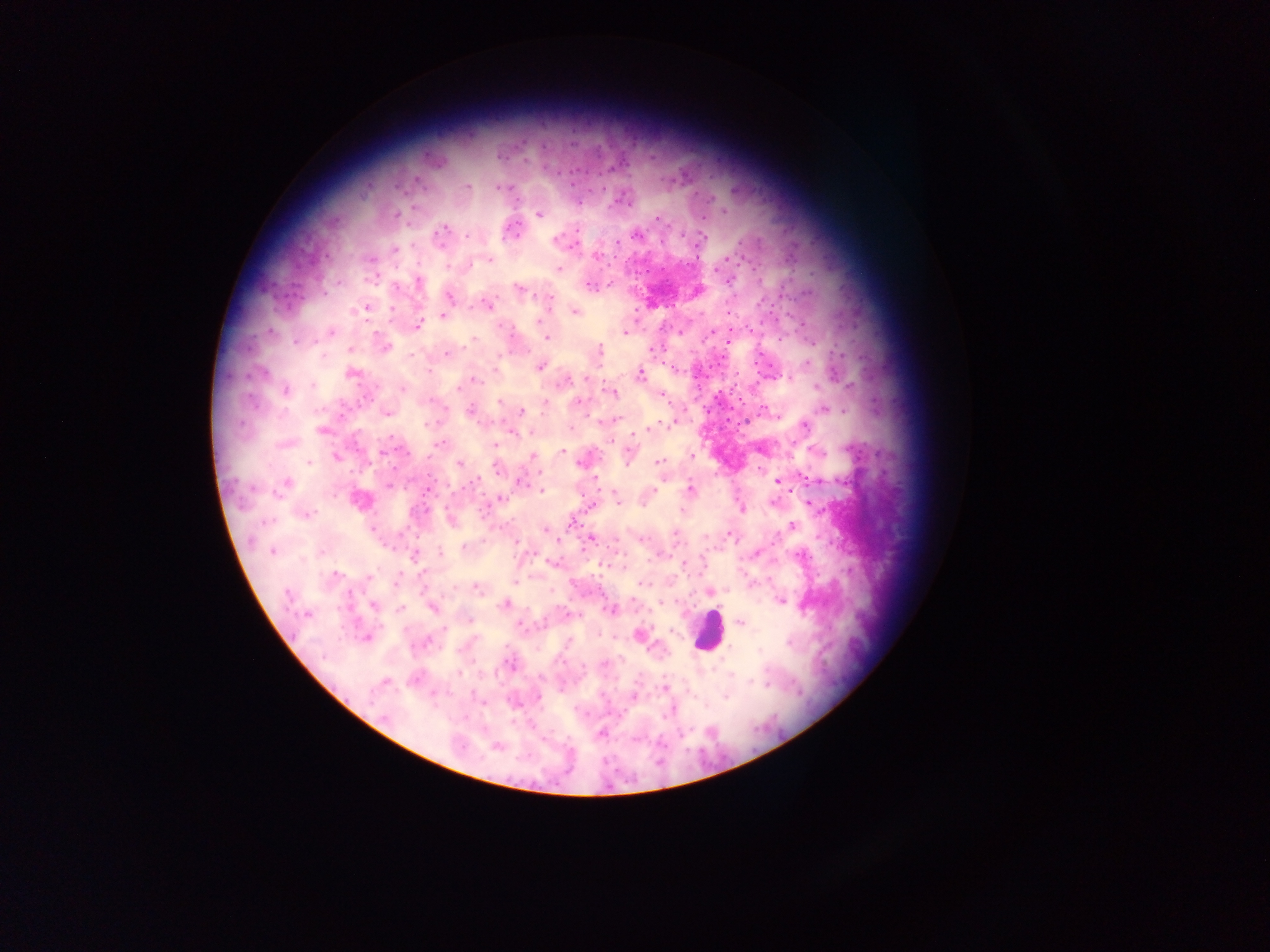 Approximate centers as (x, y) in pixels. Plasmodium parasite locations: (498, 156), (415, 179), (467, 187), (497, 187), (414, 208), (539, 214), (396, 216), (657, 218), (446, 228), (578, 230), (635, 234), (438, 237), (467, 237), (701, 238), (556, 240), (617, 243), (411, 245), (395, 248), (597, 256), (370, 259), (725, 259), (489, 260), (471, 264), (447, 266), (559, 269), (728, 281), (418, 282), (589, 286), (518, 288), (449, 296), (549, 298), (487, 305), (365, 309), (392, 309), (575, 312), (442, 316), (539, 321), (417, 326), (503, 327), (625, 332), (331, 333), (710, 333), (546, 338), (472, 340), (295, 342), (384, 348), (350, 349), (599, 352), (447, 354), (322, 356), (410, 356), (499, 357), (807, 364), (541, 366), (352, 374), (640, 374), (585, 378), (787, 378), (474, 380), (566, 381), (313, 384), (815, 386), (849, 386), (459, 388), (403, 389), (286, 391), (611, 392), (661, 395), (432, 399), (499, 402), (577, 402), (545, 404), (823, 409), (470, 411), (521, 411), (387, 414), (615, 420), (430, 423), (667, 423), (805, 426), (647, 428), (321, 430), (284, 444), (439, 444), (495, 445), (563, 451), (815, 452), (383, 453), (692, 455), (532, 456), (628, 456), (337, 458), (658, 461), (309, 462), (579, 462), (460, 464), (497, 469), (595, 478), (803, 478), (808, 480), (522, 481), (777, 481), (475, 482), (285, 483), (388, 484), (428, 488), (690, 489), (278, 490), (542, 491), (654, 491), (501, 499), (618, 500), (772, 502), (808, 504), (742, 508), (681, 510), (306, 514), (451, 521), (793, 526), (545, 530), (675, 534), (729, 534), (643, 538), (591, 539), (516, 543), (464, 547), (272, 551), (441, 552), (756, 553), (799, 555), (413, 556), (683, 564), (336, 574), (369, 576), (395, 583), (643, 584), (477, 589), (710, 592), (287, 595), (781, 600), (506, 604), (661, 604), (373, 605), (432, 608), (400, 609), (610, 610), (307, 615), (470, 620), (740, 623), (520, 625), (445, 628), (640, 634), (366, 637), (568, 642), (788, 643), (759, 651), (512, 663), (604, 663), (459, 673), (385, 681), (752, 681), (765, 685), (664, 688), (633, 696), (538, 697), (726, 697), (384, 717), (601, 734), (496, 746). Leukocyte locations: (708, 629). Collected in Ghana. Thick blood smear. One field of view. Mobile-phone photograph taken through the microscope. Image is 1270×952 pixels.